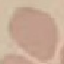
Result: negative for malaria parasites. Giemsa stain. Photographed with a smartphone camera at the microscope eyepiece. Automatically extracted cell patch, resized to 64 × 64 pixels. Thin blood smear.